Classify this cell by malaria status.
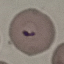
Parasitized.

Summary:
  - Stain: Giemsa
  - Preparation: thin blood film
  - Image type: automatically extracted cell patch, resized to 64 × 64 pixels
  - Capture: smartphone through the microscope eyepiece